Locate every Plasmodium parasite.
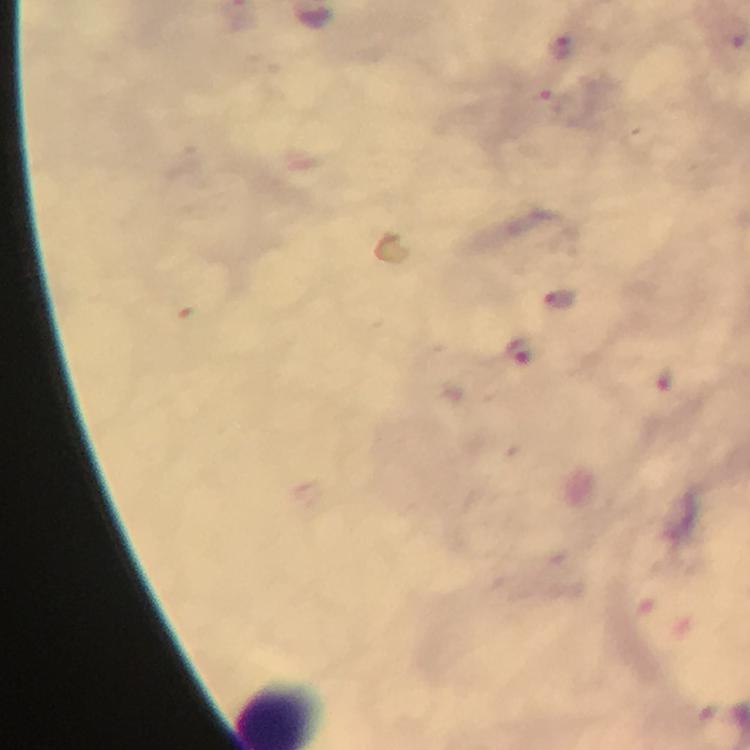

Approximate centers as {x, y} in pixels.
Plasmodium parasites: {560, 49}, {559, 297}, {519, 348}.

{
  "context": "from a malaria diagnostic workup",
  "preparation": "thick smear",
  "magnification": "100x",
  "cropped_from": "one field of view",
  "stain": "Giemsa",
  "immersion_oil": "applied",
  "capture": "smartphone photograph through a microscope",
  "image_size": "750×750 pixels"
}